Outline each Plasmodium falciparum-infected red blood cell.
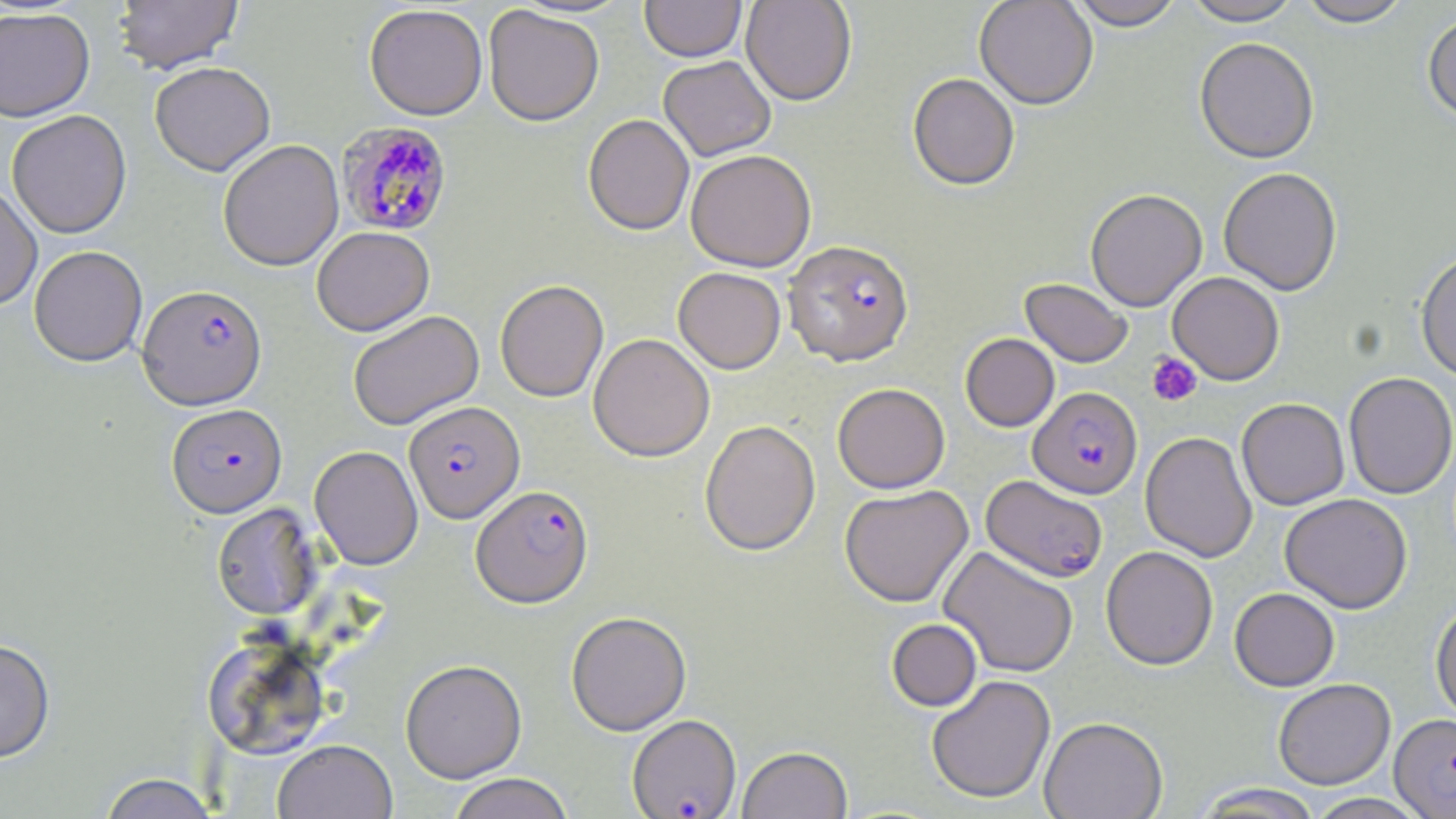
Approximate bounding boxes as (x1, y1, x2, y2) in pixels.
Plasmodium falciparum-infected red blood cells: (336, 121, 455, 237), (783, 240, 914, 366), (137, 284, 267, 410), (1028, 387, 1142, 499), (404, 401, 525, 523), (166, 403, 287, 517), (980, 475, 1108, 582), (471, 484, 593, 607), (627, 714, 741, 818), (1390, 714, 1456, 817).

Summary:
  - Platelet locations: (1146, 352, 1203, 407)
  - Uninfected red blood cell locations: (112, 0, 243, 74), (640, 0, 746, 62), (741, 0, 857, 106), (974, 0, 1097, 109), (1068, 0, 1185, 31), (1181, 0, 1305, 26), (1296, 0, 1413, 27), (364, 4, 488, 121), (483, 5, 604, 126), (0, 7, 95, 121), (1422, 12, 1456, 126), (1195, 38, 1319, 164), (659, 56, 776, 161), (150, 61, 275, 176), (907, 73, 1020, 191), (6, 110, 131, 238), (583, 115, 694, 236), (218, 140, 343, 271), (686, 150, 816, 271), (1218, 167, 1342, 295), (0, 181, 42, 310), (1085, 189, 1207, 311), (312, 227, 434, 336), (29, 245, 147, 366), (1416, 250, 1456, 382), (673, 267, 786, 374), (1167, 272, 1284, 385), (1020, 278, 1133, 367), (495, 280, 609, 402), (348, 310, 484, 430), (588, 333, 715, 462), (960, 333, 1060, 431), (1343, 372, 1456, 499), (832, 383, 950, 493), (1237, 398, 1349, 510), (700, 420, 820, 556), (1140, 431, 1257, 562), (309, 445, 423, 570), (839, 485, 973, 608), (1279, 493, 1412, 613), (212, 502, 322, 621), (1101, 546, 1218, 670), (936, 547, 1076, 679), (1229, 587, 1339, 691), (1431, 599, 1456, 724), (566, 611, 691, 735), (887, 619, 982, 711), (201, 635, 330, 760), (0, 638, 55, 763), (400, 660, 527, 782), (926, 674, 1056, 804), (1273, 678, 1395, 789), (1039, 716, 1167, 819), (273, 739, 398, 819), (738, 745, 852, 819), (97, 773, 220, 819), (446, 773, 576, 819), (1191, 783, 1325, 818), (1306, 793, 1429, 819)
  - Slide-level diagnosis: Plasmodium falciparum
  - Stain: May-Grünwald-Giemsa
  - Image size: 1456×819 pixels
  - Preparation: thin blood film
  - Field of view: single
  - Modality: light microscopy
  - Magnification: 1000x